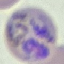 Result: malaria parasites identified. Acquired by smartphone through the microscope eyepiece. Cell patch, automatically extracted from a larger field of view and resized to 64 × 64 pixels. Giemsa-stained preparation. Thin smear of blood.